Point out each leukocyte.
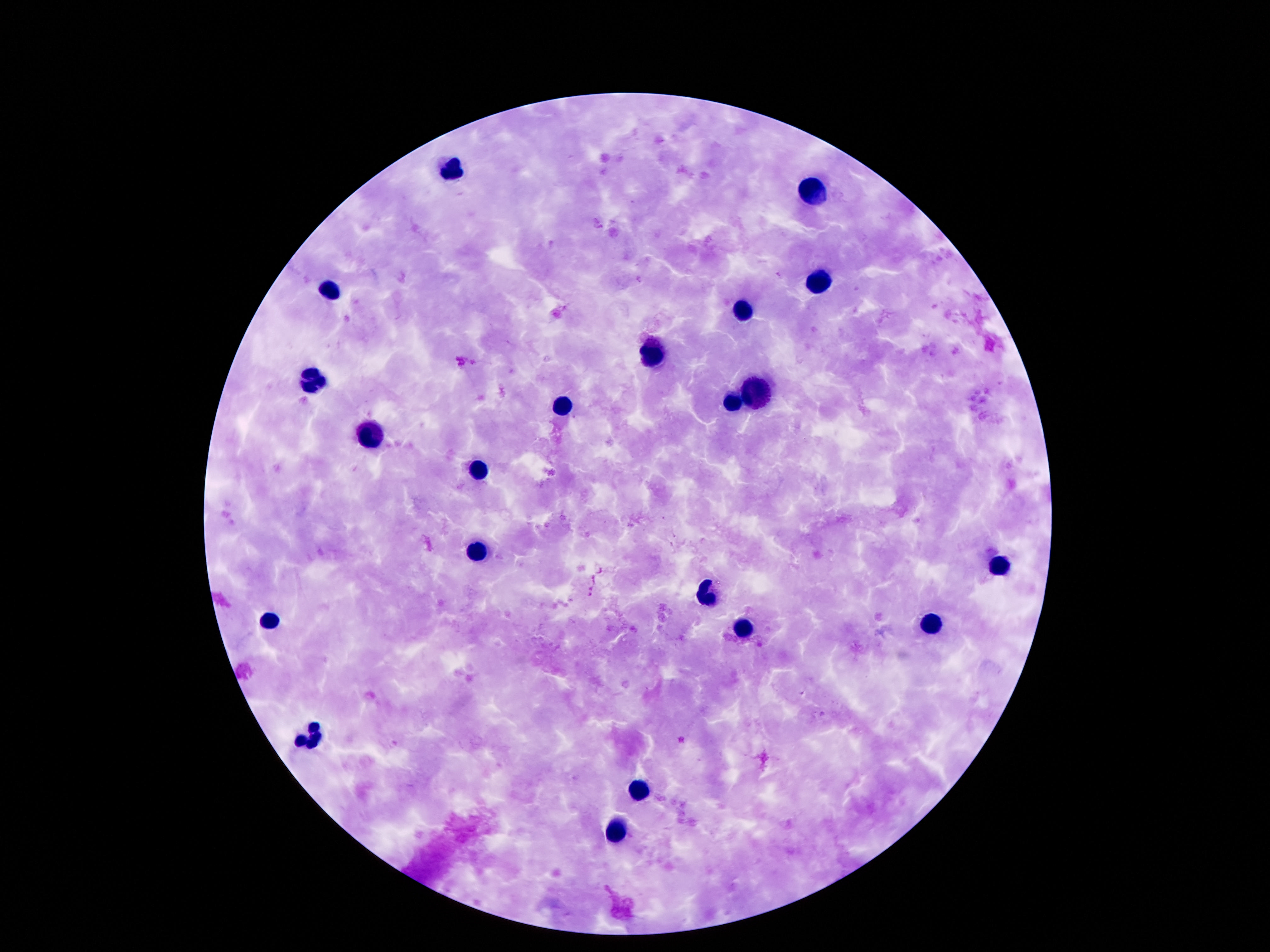
Approximate centers as {x, y} in pixels.
Leukocytes: {452, 167}, {816, 192}, {816, 282}, {327, 290}, {741, 315}, {650, 356}, {314, 380}, {755, 393}, {734, 401}, {560, 406}, {370, 439}, {480, 468}, {478, 554}, {999, 567}, {710, 595}, {269, 618}, {933, 625}, {743, 626}, {308, 735}, {640, 789}, {616, 832}.

field of view = one from this slide
image size = 1270×952 pixels
magnification = 100x
stain = Giemsa
capture = smartphone camera through the microscope eyepiece
preparation = thick blood film
patient malaria status = uninfected